Report the malaria status of this cell.
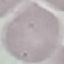
It is uninfected.

Summary:
  - Image type: automatically extracted cell patch, resized to 64 × 64 pixels
  - Stain: Giemsa
  - Preparation: thin blood film
  - Capture: smartphone camera at the microscope eyepiece